Outline each blood parasite and name the species.
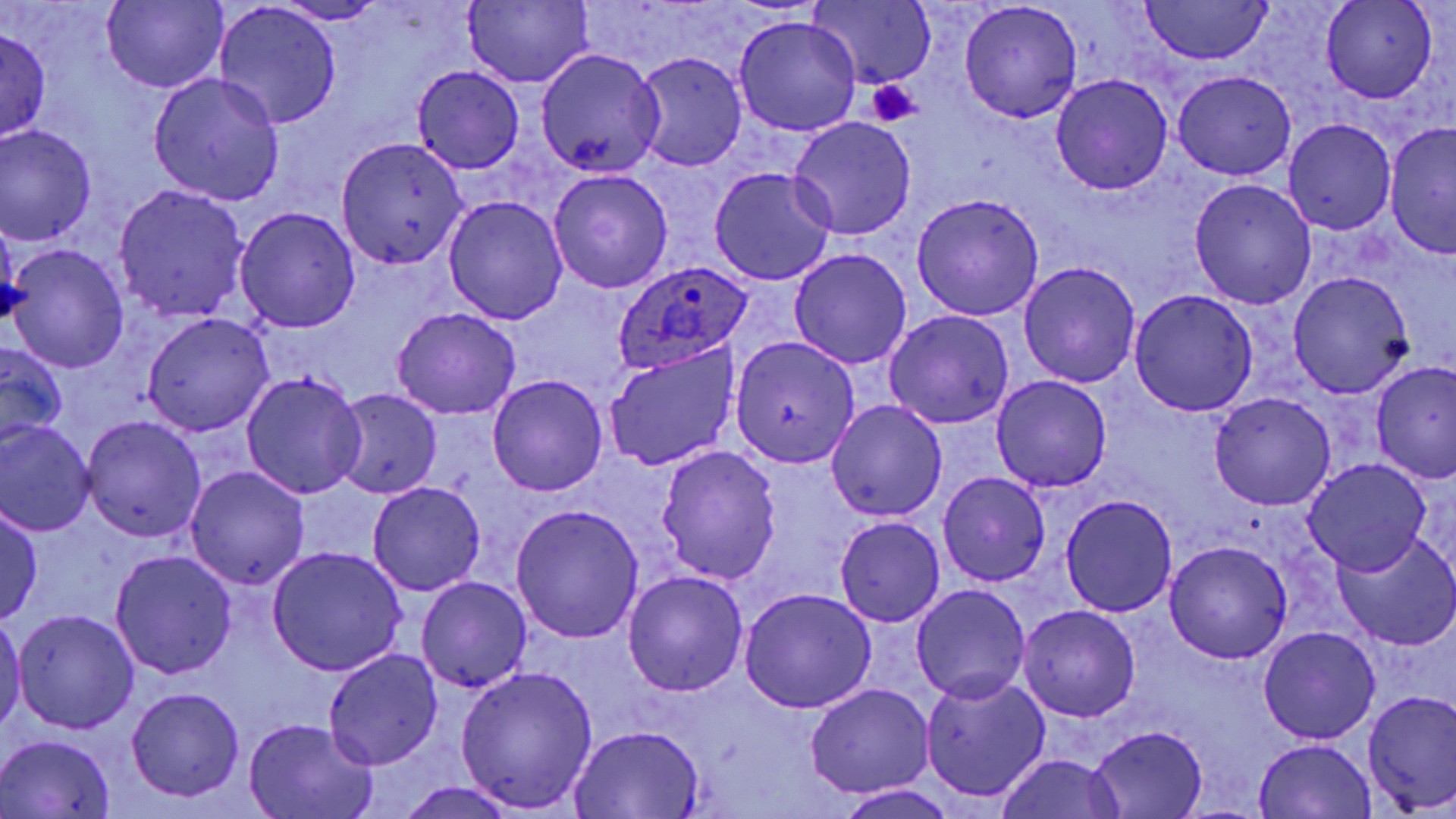
Approximate bounding boxes as [x1, y1, x2, y2] in pixels.
Plasmodium ovale-infected red blood cells: [613, 260, 754, 373].
No Plasmodium falciparum, Plasmodium malariae, Plasmodium vivax, Babesia divergens, or Trypanosoma brucei observed.

Summary:
  - Platelet locations: [865, 78, 924, 126]
  - Uninfected red blood cell locations: [805, 0, 936, 90], [1321, 0, 1437, 103], [101, 2, 227, 92], [278, 2, 390, 24], [463, 2, 593, 88], [1138, 2, 1273, 64], [216, 3, 342, 129], [959, 3, 1083, 122], [733, 15, 862, 138], [0, 28, 51, 142], [535, 48, 665, 176], [633, 51, 748, 173], [413, 66, 524, 173], [1173, 69, 1294, 179], [148, 72, 285, 205], [1051, 73, 1173, 195], [788, 117, 917, 241], [1283, 119, 1397, 235], [1385, 122, 1456, 256], [0, 125, 96, 245], [336, 136, 467, 268], [708, 166, 837, 287], [547, 170, 674, 294], [1188, 179, 1317, 309], [114, 185, 250, 323], [912, 193, 1044, 320], [443, 195, 568, 325], [234, 207, 361, 334], [0, 213, 25, 332], [4, 243, 129, 372], [789, 248, 912, 369], [1018, 261, 1141, 388], [1287, 271, 1414, 399], [1129, 289, 1259, 414], [391, 307, 521, 420], [883, 309, 1015, 430], [142, 312, 274, 436], [732, 335, 860, 468], [0, 340, 68, 450], [602, 344, 740, 471], [1371, 360, 1455, 486], [241, 371, 366, 499], [489, 375, 607, 495], [991, 375, 1111, 494], [332, 389, 442, 500], [1210, 392, 1334, 510], [825, 399, 948, 522], [80, 415, 207, 543], [0, 420, 96, 536], [656, 446, 782, 586], [1303, 459, 1432, 577], [185, 465, 310, 591], [939, 470, 1050, 587], [368, 481, 486, 596], [1061, 494, 1178, 616], [0, 504, 44, 624], [510, 504, 643, 641], [306, 511, 457, 644], [834, 515, 946, 627], [1331, 530, 1456, 652], [1164, 539, 1293, 663], [267, 547, 407, 676], [109, 550, 237, 679], [622, 571, 748, 697], [416, 578, 531, 693], [911, 584, 1031, 705], [739, 590, 877, 713], [1018, 605, 1141, 722], [13, 609, 140, 734], [0, 614, 26, 735], [1259, 628, 1379, 744], [323, 648, 444, 771], [454, 665, 598, 814], [921, 674, 1050, 802], [805, 683, 934, 798], [126, 687, 244, 800], [1362, 689, 1456, 815], [244, 718, 381, 818], [570, 725, 704, 816], [1090, 726, 1209, 817], [2, 734, 116, 816], [1253, 738, 1378, 818], [994, 753, 1127, 819], [396, 779, 519, 819], [833, 783, 959, 818]
  - Slide-level diagnosis: Plasmodium ovale
  - Magnification: 1000x
  - Field of view: single
  - Image size: 1456×819 pixels
  - Modality: optical microscopy
  - Preparation: thin blood film
  - Stain: May-Grünwald-Giemsa